Draw a bounding box around every artifact (stain precipitate or debris).
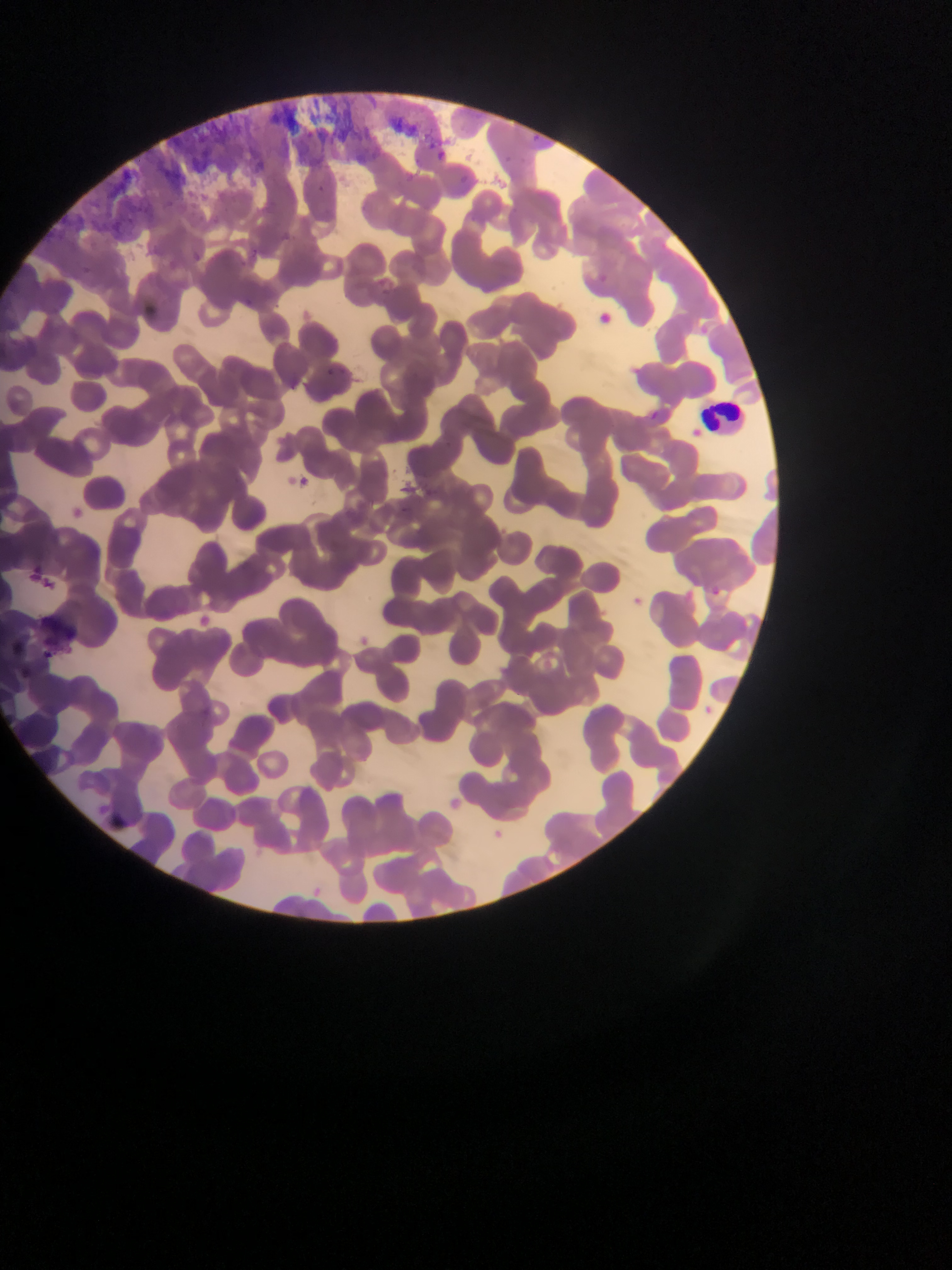

Approximate bounding boxes as (left, top, right, bottom) in pixels.
Artifacts (stain precipitate or debris): (32, 612, 79, 648).

Leukocyte locations: (702, 398, 742, 433). Malaria parasite locations: (327, 364, 339, 378), (650, 405, 659, 422), (434, 436, 476, 465), (290, 474, 318, 488), (420, 483, 439, 503), (43, 578, 60, 604), (704, 586, 724, 607), (486, 824, 508, 844). Photographed through a microscope with a mobile-phone camera. Image is 952×1270 pixels. Collected in Ghana. Thin blood film. One field of view.